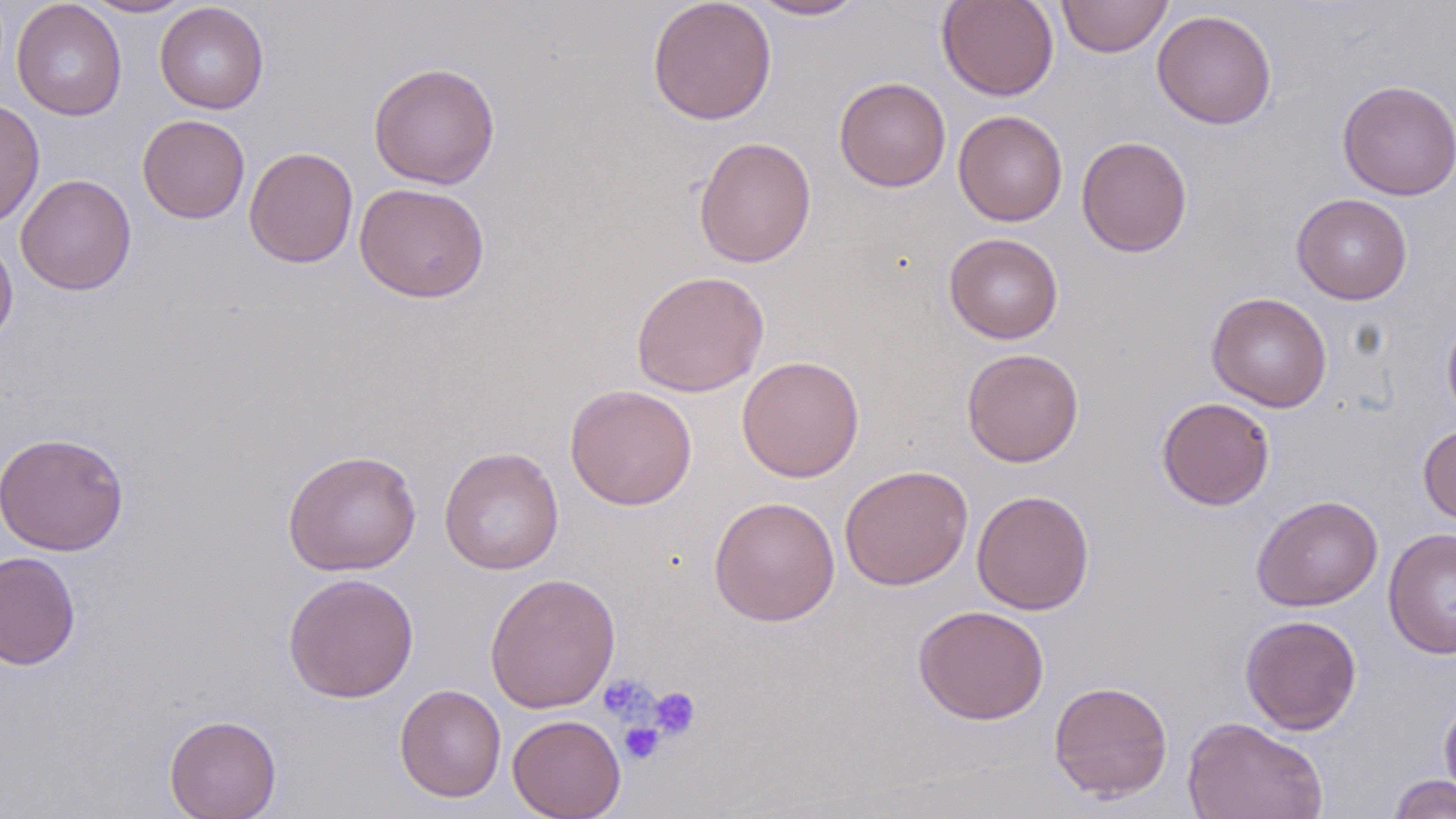

Summary:
  - Coordinate format: approximate bounding boxes as (x1,y1)-(x2,y2) corner pairs in pixels
  - Platelet locations: (598,674)-(657,724), (647,686)-(701,742), (619,721)-(665,765)
  - Uninfected red blood cell locations: (80,0)-(196,18), (647,0)-(777,125), (746,0)-(870,20), (936,0)-(1059,101), (1056,0)-(1173,57), (12,1)-(127,121), (155,2)-(269,114), (1152,9)-(1277,129), (368,62)-(500,188), (834,76)-(951,192), (1336,80)-(1456,200), (0,99)-(45,228), (953,109)-(1068,226), (137,114)-(251,224), (693,136)-(817,268), (1077,136)-(1193,257), (244,147)-(359,268), (15,174)-(137,295), (354,182)-(490,303), (1291,193)-(1413,305), (943,233)-(1064,344), (0,234)-(18,348), (631,270)-(769,397), (1206,292)-(1332,412), (1441,311)-(1456,429), (961,348)-(1084,467), (736,355)-(865,482), (565,384)-(697,510), (1157,397)-(1275,510), (1418,423)-(1456,525), (0,431)-(129,556), (439,447)-(564,575), (282,449)-(422,575), (839,464)-(974,591), (971,490)-(1095,615), (1250,495)-(1383,612), (708,496)-(841,626), (1383,527)-(1456,659), (0,551)-(81,670), (282,571)-(420,703), (484,572)-(621,714), (913,605)-(1050,724), (1240,614)-(1363,735), (1049,680)-(1173,801), (395,684)-(506,802), (1438,692)-(1456,810), (164,714)-(282,819), (507,714)-(626,819), (1182,716)-(1328,818), (1388,773)-(1456,819)
  - Slide-level diagnosis: no evidence of blood parasites
  - Field of view: single
  - Image size: 1456×819 pixels
  - Modality: optical microscopy
  - Stain: May-Grünwald-Giemsa
  - Preparation: thin blood smear
  - Magnification: 1000x